Report the malaria status of this cell.
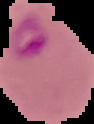
Parasitized.

preparation = thin blood smear
image size = 94×124 pixels
image type = segmented cell region with the area outside set to black